Report the malaria status of this cell.
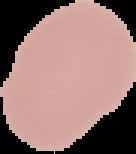

It is uninfected.

Image is 136×154 pixels. From a thin blood smear. Segmented cell region on a black background.